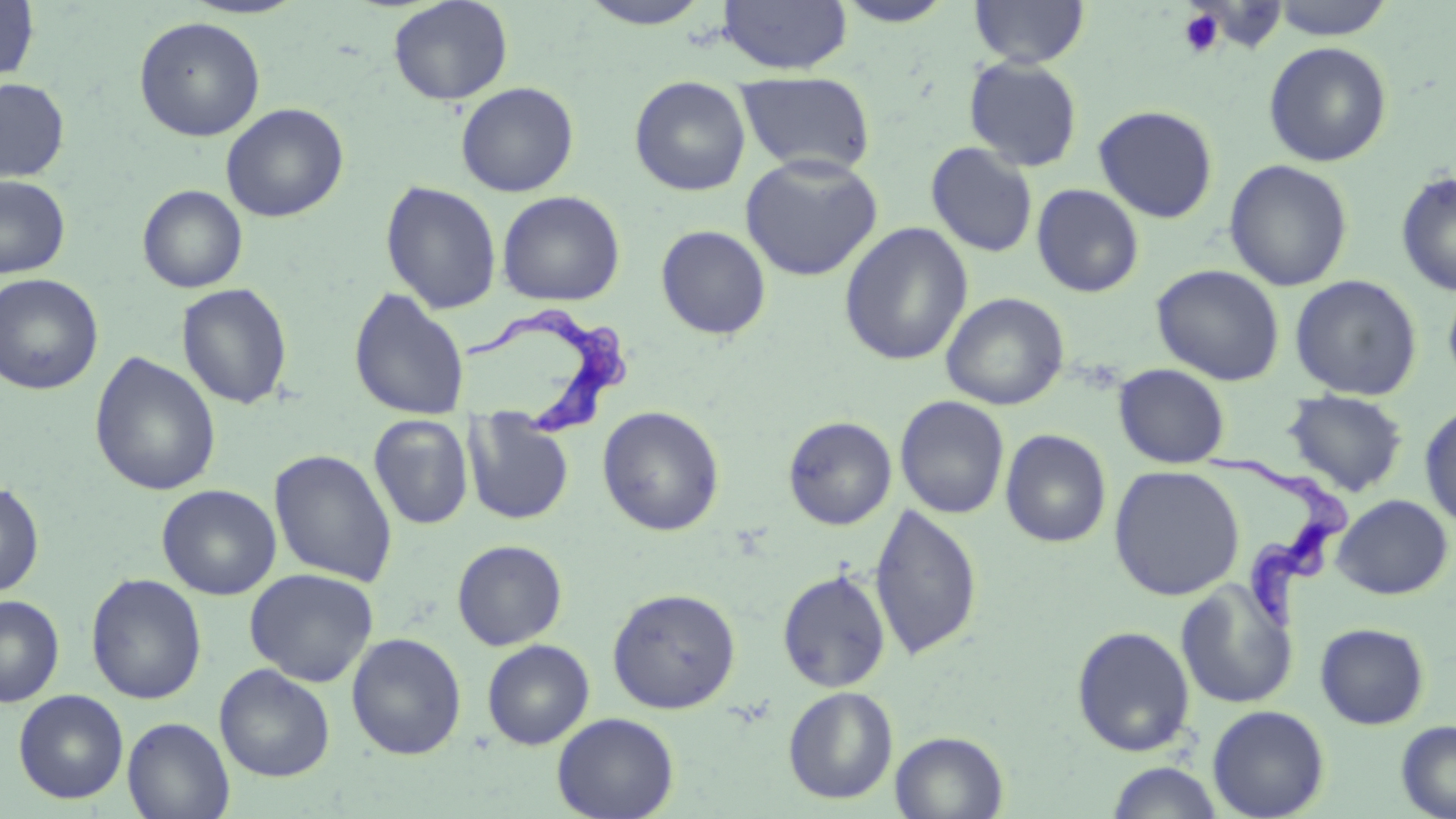

slide_level_diagnosis: Trypanosoma brucei
image_size: 1456×819 pixels
modality: optical microscopy
trypanosoma_brucei_locations: 'approximate bounding boxes as [x1, y1, x2, y2] in pixels: [464, 305, 633, 442], [1208, 451, 1350, 637]'
field_of_view: single
uninfected_red_blood_cell_locations: 'approximate bounding boxes as [x1, y1, x2, y2] in pixels: [0, 0, 39, 84], [180, 0, 309, 20], [387, 0, 514, 106], [576, 0, 714, 29], [833, 0, 957, 27], [969, 0, 1090, 68], [1268, 0, 1395, 40], [717, 1, 852, 75], [133, 16, 266, 142], [1263, 41, 1392, 167], [963, 57, 1083, 172], [736, 71, 877, 177], [629, 76, 751, 196], [0, 77, 70, 183], [455, 81, 579, 197], [221, 103, 349, 223], [1092, 105, 1219, 224], [925, 142, 1038, 258], [740, 154, 883, 281], [1223, 159, 1354, 291], [1396, 171, 1456, 297], [0, 175, 71, 279], [380, 181, 502, 315], [137, 184, 248, 293], [1031, 184, 1144, 298], [497, 190, 625, 306], [838, 223, 974, 367], [656, 225, 771, 340], [1150, 263, 1286, 386], [0, 274, 103, 395], [1289, 274, 1422, 400], [1442, 278, 1456, 391], [176, 283, 293, 410], [349, 288, 470, 421], [941, 292, 1069, 410], [89, 351, 221, 496], [1113, 363, 1230, 468], [1283, 391, 1408, 496], [895, 395, 1010, 519], [1419, 403, 1456, 530], [597, 405, 725, 536], [464, 411, 574, 525], [368, 414, 474, 530], [783, 415, 897, 530], [1000, 429, 1111, 548], [268, 448, 398, 587], [1109, 465, 1244, 601], [0, 480, 44, 598], [157, 484, 282, 600], [1331, 494, 1453, 599], [869, 502, 982, 662], [452, 539, 568, 650], [244, 567, 379, 686], [777, 569, 891, 693], [86, 573, 207, 705], [1174, 579, 1298, 710], [607, 587, 741, 714], [0, 595, 64, 707], [1314, 623, 1429, 729], [1070, 624, 1196, 757], [346, 632, 467, 760], [482, 639, 595, 750], [214, 663, 335, 782], [783, 686, 899, 804], [13, 689, 128, 803], [1207, 704, 1330, 818], [552, 712, 679, 819], [122, 716, 234, 819], [1396, 719, 1456, 819], [890, 731, 1008, 819], [1105, 762, 1226, 819]'
preparation: thin blood smear
magnification: 1000x
platelet_locations: 'approximate bounding boxes as [x1, y1, x2, y2] in pixels: [1178, 8, 1226, 58]'
stain: May-Grünwald-Giemsa